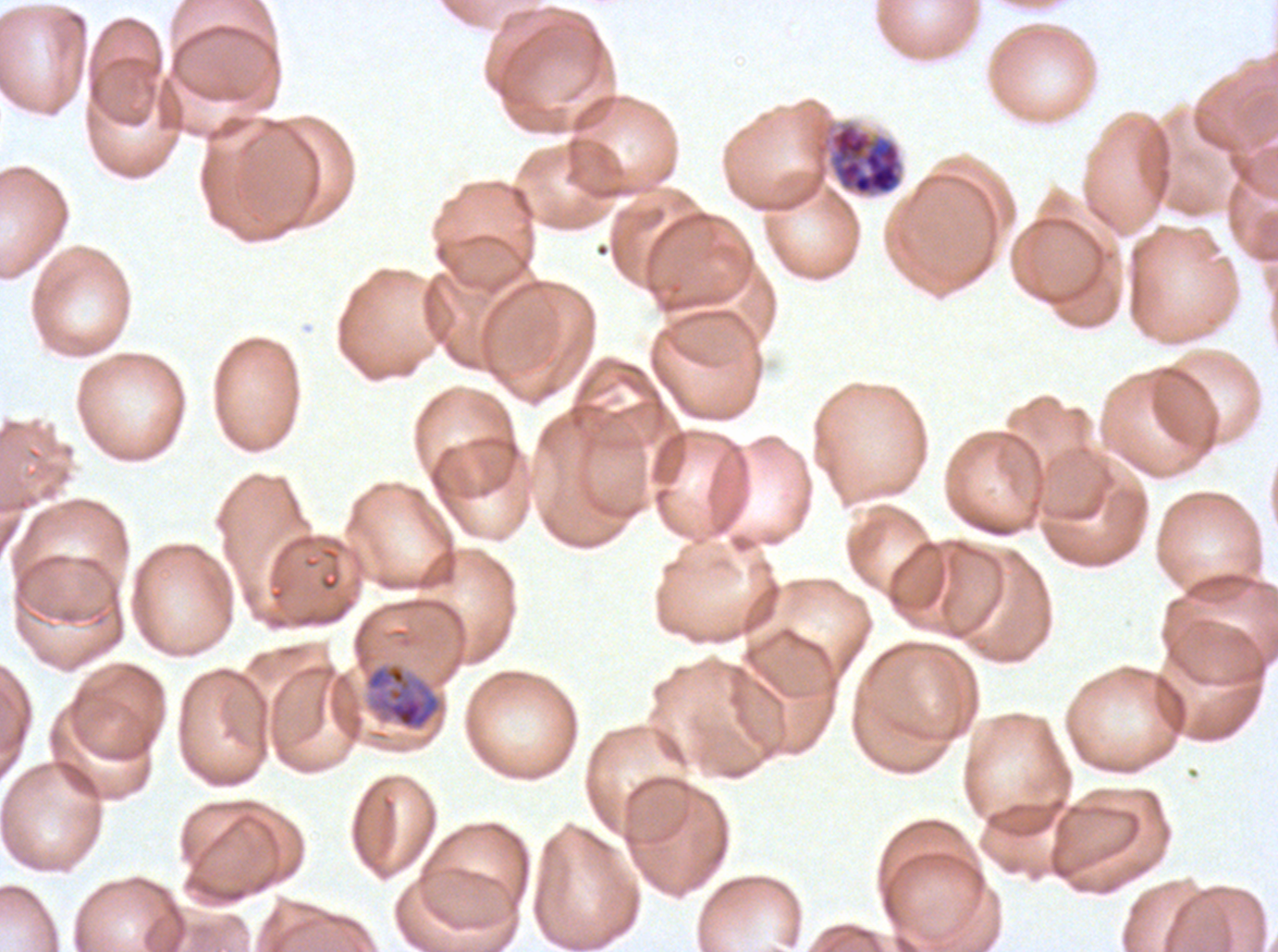

Approximate bounding rectangles given as corner coordinates in pixels from the top-left. Late schizont locations: (x1=828, y1=121, x2=904, y2=197). Late trophozoite locations: (x1=363, y1=662, x2=444, y2=732). Ex-vivo Plasmodium falciparum culture from a patient in The Gambia, grown for 24 to 48 hours. Giemsa stain. A sub-image separated from a larger composite. Thin blood smear. Life-cycle stages observed: late trophozoite, late schizont. Image is 1278×952 pixels.